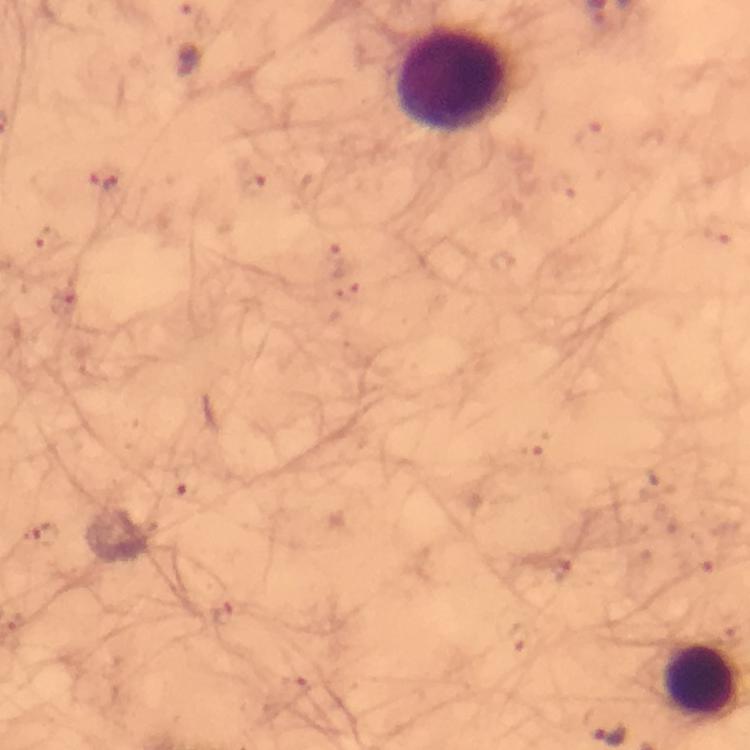

Approximate object centers, in pixels from the top-left corner. Leukocyte locations: (x=454, y=80), (x=701, y=680). Plasmodium parasite locations: (x=594, y=138), (x=105, y=180), (x=720, y=229), (x=47, y=241), (x=334, y=253), (x=349, y=292), (x=63, y=303), (x=531, y=442), (x=187, y=480), (x=42, y=537), (x=700, y=561), (x=559, y=570), (x=222, y=614), (x=515, y=637), (x=294, y=692). Photographed with a smartphone mounted on the microscope. 100x magnification. Giemsa stain. Cropped region of a single field of view. Thick blood film. Immersion oil applied. Image is 750×750 pixels. From a malaria diagnostic workup.